Assess this cell for malaria.
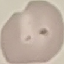
It is uninfected.

Summary:
  - Image type: automatically extracted cell patch, resized to 64 × 64 pixels
  - Capture: smartphone through the microscope eyepiece
  - Stain: Giemsa
  - Preparation: thin blood smear